Locate every Plasmodium falciparum-infected red blood cell.
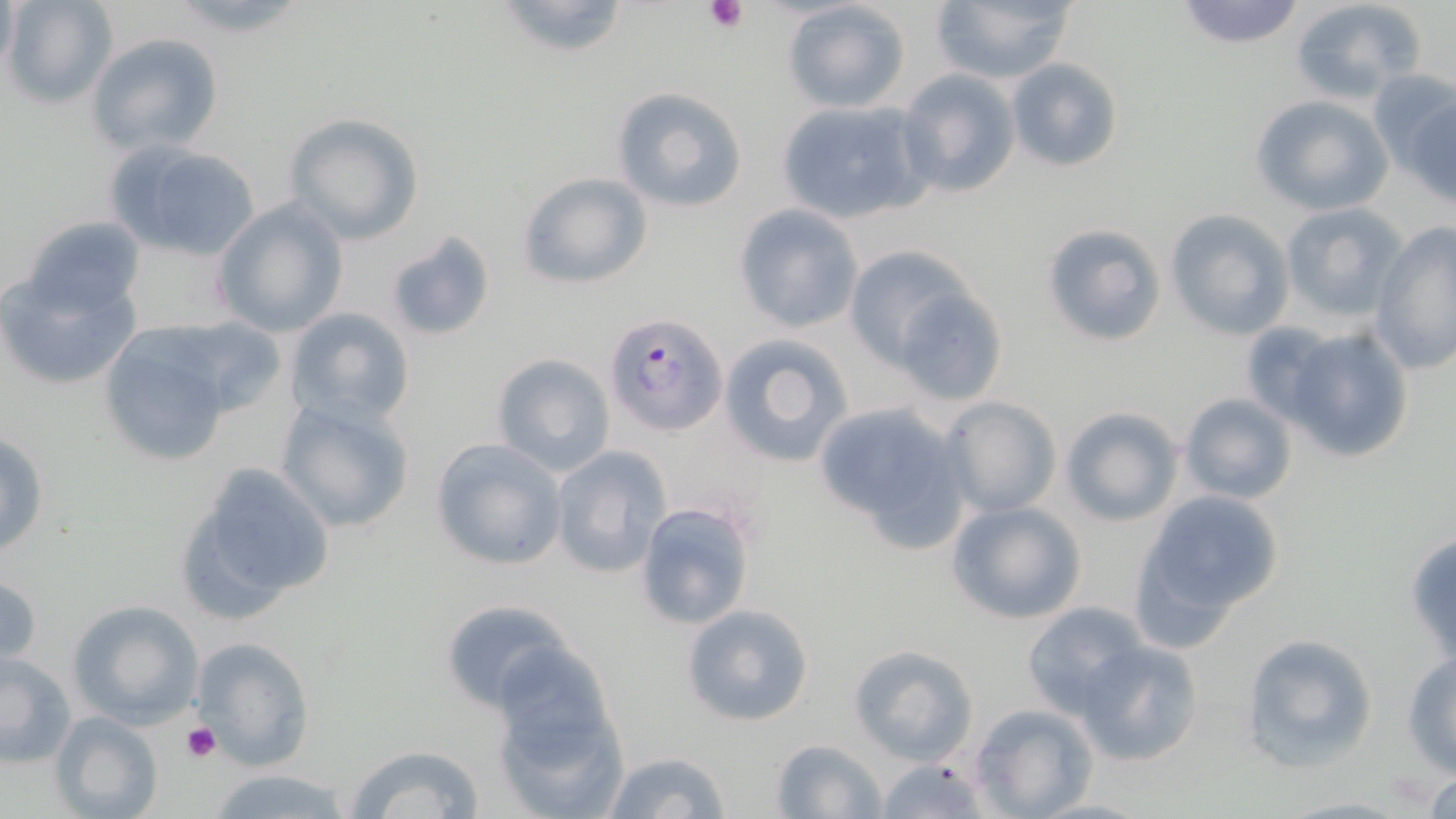
Approximate bounding boxes as (x1, y1, x2, y2) in pixels.
Plasmodium falciparum-infected red blood cells: (604, 311, 727, 436).

slide_level_diagnosis: Plasmodium falciparum
stain: May-Grünwald-Giemsa
preparation: thin blood smear
magnification: 1000x
image_size: 1456×819 pixels
uninfected_red_blood_cell_locations: 'approximate bounding boxes as (x1, y1, x2, y2) in pixels: (2, 0, 117, 108), (490, 0, 634, 59), (781, 0, 913, 114), (929, 0, 1079, 85), (1172, 0, 1307, 49), (1288, 0, 1426, 103), (85, 32, 224, 156), (1005, 57, 1123, 173), (897, 69, 1021, 199), (1398, 84, 1456, 204), (610, 86, 749, 213), (1249, 94, 1394, 216), (775, 99, 932, 224), (281, 112, 423, 244), (103, 138, 265, 261), (516, 171, 652, 289), (210, 199, 349, 339), (1278, 201, 1409, 323), (732, 204, 865, 335), (1163, 209, 1293, 340), (15, 215, 146, 319), (1042, 221, 1166, 347), (1369, 221, 1456, 377), (384, 230, 495, 343), (842, 245, 983, 371), (0, 264, 144, 392), (889, 283, 1009, 406), (283, 307, 415, 430), (95, 322, 247, 467), (1238, 322, 1350, 427), (1281, 325, 1414, 464), (718, 332, 854, 468), (491, 352, 616, 476), (1177, 391, 1300, 505), (940, 396, 1062, 517), (275, 397, 414, 534), (811, 401, 970, 549), (1057, 407, 1183, 527), (0, 431, 50, 559), (430, 439, 566, 572), (549, 444, 671, 578), (171, 458, 338, 622), (1135, 489, 1285, 627), (633, 498, 757, 631), (946, 500, 1086, 625), (1404, 532, 1456, 667), (0, 572, 42, 672), (438, 596, 578, 718), (66, 599, 204, 730), (1021, 601, 1147, 719), (680, 603, 814, 726), (1240, 634, 1376, 768), (190, 635, 316, 769), (1075, 639, 1205, 765), (848, 643, 979, 766), (1402, 650, 1456, 775), (0, 652, 76, 767), (491, 674, 629, 817), (972, 703, 1097, 819), (48, 710, 163, 819), (769, 739, 885, 819), (346, 744, 489, 819), (599, 750, 732, 819), (877, 759, 989, 819), (202, 767, 360, 819), (1417, 767, 1456, 819)'
platelet_locations: 'approximate bounding boxes as (x1, y1, x2, y2) in pixels: (703, 0, 749, 32), (182, 722, 221, 764)'
field_of_view: one of a larger specimen
modality: light microscopy